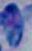
modality: micrograph
identification: Toxoplasma gondii
magnification: 1000x